Report the malaria status of this cell.
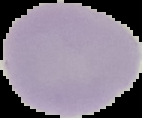

It is uninfected.

Summary:
  - Image type: segmented cell region on a black background
  - Preparation: thin blood film
  - Image size: 142×118 pixels